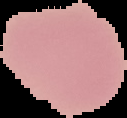

image_size: 127×118 pixels
preparation: thin blood film
result: no Plasmodium parasites seen
image_type: segmented cell region with the area outside set to black